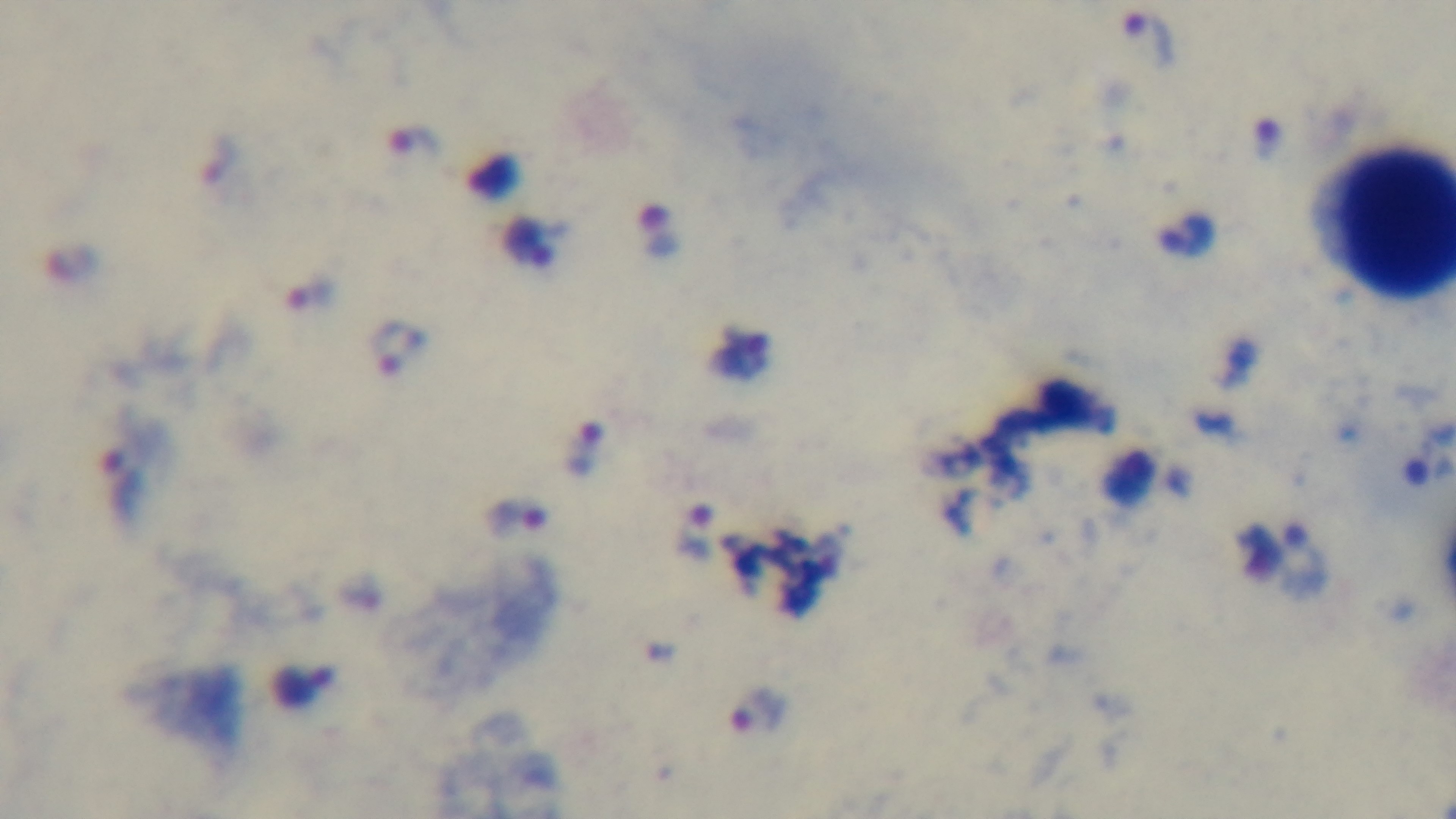
100x oil-immersion objective. Light microscopy. One field from the slide. Malaria status: positive. Giemsa stain. Mounted 4K digital camera. Preparation: thick smear.